Name the cell type shown.
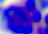
This is a leukocyte.

Summary:
  - Modality: photomicrograph
  - Magnification: 400x